Describe the morphology of the red blood cells.
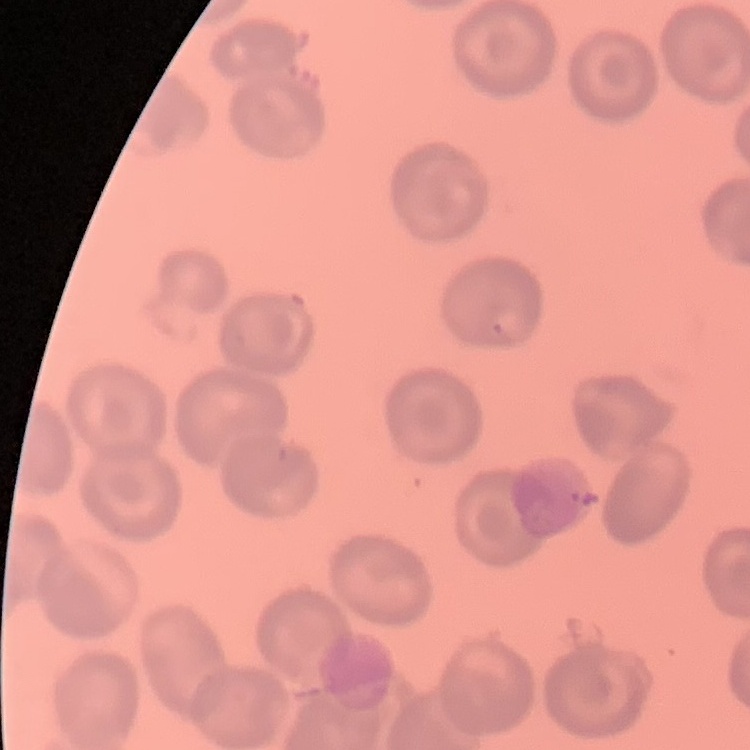
They show no rouleaux formation.

stain = Field's or Giemsa
image type = square crop of a larger photomicrograph
preparation = thin blood film